Outline each Plasmodium falciparum-infected red blood cell.
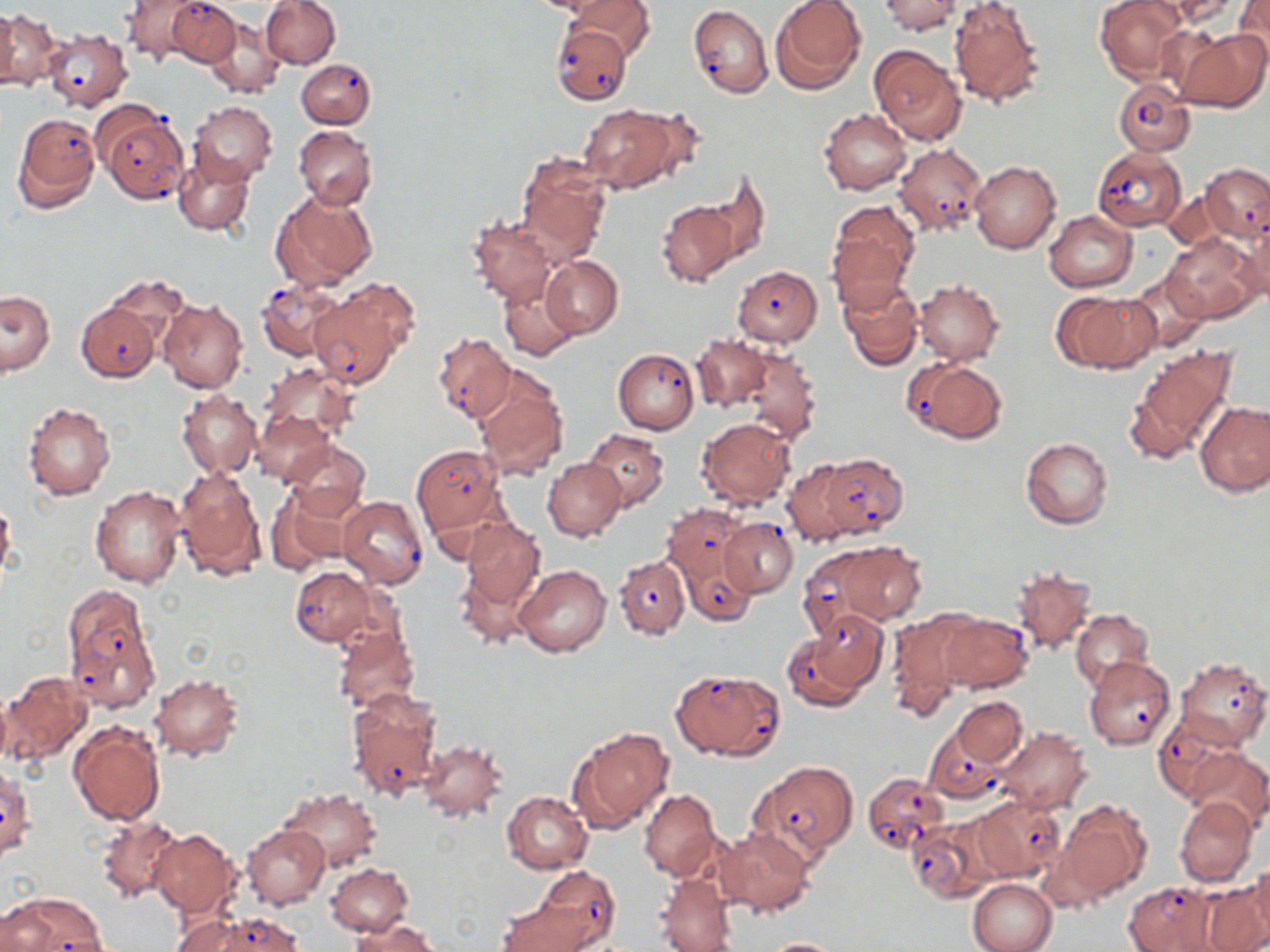

Approximate bounding boxes as (x1,y1)-(x2,y2) corner pairs in pixels.
Plasmodium falciparum-infected red blood cells: (166,0)-(240,66), (687,4)-(772,98), (551,23)-(631,105), (42,27)-(133,111), (297,58)-(376,128), (1113,79)-(1195,156), (97,106)-(188,203), (11,112)-(100,212), (894,143)-(988,235), (1092,147)-(1186,232), (1198,163)-(1269,243), (733,265)-(822,346), (256,277)-(348,360), (310,284)-(411,385), (74,301)-(161,382), (433,332)-(515,425), (613,349)-(699,434), (903,358)-(1007,445), (412,445)-(504,533), (816,453)-(906,539), (338,495)-(429,589), (662,503)-(747,587), (719,518)-(798,598), (678,553)-(758,627), (806,553)-(887,645), (614,556)-(689,640), (290,566)-(378,647), (61,582)-(158,709), (798,611)-(887,702), (936,613)-(1033,693), (1084,655)-(1177,750), (1176,657)-(1269,748), (671,668)-(782,762), (346,687)-(445,801), (1152,714)-(1241,802), (923,727)-(1008,802), (751,760)-(857,864), (862,772)-(948,853), (967,795)-(1064,881), (905,819)-(997,902), (531,866)-(620,949), (1123,883)-(1216,952), (5,892)-(107,951), (184,911)-(305,952).

Uninfected red blood cell locations: (119,0)-(208,65), (261,0)-(340,69), (568,0)-(656,62), (770,0)-(866,93), (880,0)-(961,35), (947,0)-(1045,109), (1094,0)-(1188,83), (1144,0)-(1243,27), (1231,1)-(1270,67), (0,9)-(20,91), (1,10)-(62,92), (204,19)-(285,98), (1174,28)-(1268,113), (869,44)-(966,145), (187,101)-(277,187), (578,104)-(677,191), (631,106)-(708,185), (820,109)-(912,196), (294,126)-(378,209), (172,152)-(255,236), (517,152)-(612,261), (970,160)-(1061,253), (700,172)-(769,271), (270,188)-(376,292), (657,200)-(739,288), (826,200)-(918,303), (1043,209)-(1137,293), (467,215)-(557,307), (1237,217)-(1270,304), (1162,231)-(1263,323), (540,256)-(622,338), (1122,272)-(1207,353), (101,276)-(190,347), (838,278)-(923,371), (913,279)-(1003,365), (499,280)-(580,361), (1051,289)-(1158,374), (1,290)-(54,377), (158,300)-(248,392), (690,334)-(774,411), (1123,345)-(1240,465), (740,347)-(822,446), (261,362)-(359,441), (472,367)-(569,480), (177,391)-(260,478), (1195,400)-(1270,497), (22,401)-(116,501), (250,409)-(336,488), (697,417)-(796,508), (582,428)-(669,511), (1020,437)-(1113,530), (280,440)-(370,520), (544,458)-(626,543), (780,459)-(863,547), (175,465)-(267,583), (265,484)-(358,575), (89,486)-(187,588), (0,499)-(16,583), (460,516)-(545,612), (839,541)-(926,625), (454,559)-(540,649), (514,563)-(612,658), (1010,564)-(1096,655), (1071,609)-(1152,690), (886,611)-(975,716), (333,626)-(419,714), (1,671)-(93,770), (148,673)-(244,762), (953,696)-(1027,767), (68,721)-(165,826), (568,726)-(673,831), (997,727)-(1091,815), (417,738)-(508,821), (1184,747)-(1270,833), (1,764)-(33,860), (278,787)-(382,871), (639,788)-(719,880), (501,790)-(593,874), (1174,796)-(1258,887), (1054,800)-(1150,905), (96,814)-(185,904), (243,824)-(331,910), (714,826)-(813,917), (149,827)-(241,919), (1250,860)-(1270,944), (326,863)-(412,936), (653,874)-(738,951), (967,878)-(1057,952), (1199,880)-(1270,952), (497,899)-(594,952), (0,900)-(54,951), (353,918)-(438,952), (761,937)-(848,951). Slide-level diagnosis: Plasmodium falciparum. Image is 1270×952 pixels. 1000x magnification. Single field of view. May-Grünwald-Giemsa-stained preparation. Thin blood film. Optical microscopy.